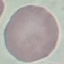

result = no malaria parasites detected
capture = smartphone camera at the microscope eyepiece
stain = Giemsa
image type = automatically extracted cell patch, resized to 64 × 64 pixels
preparation = thin blood film